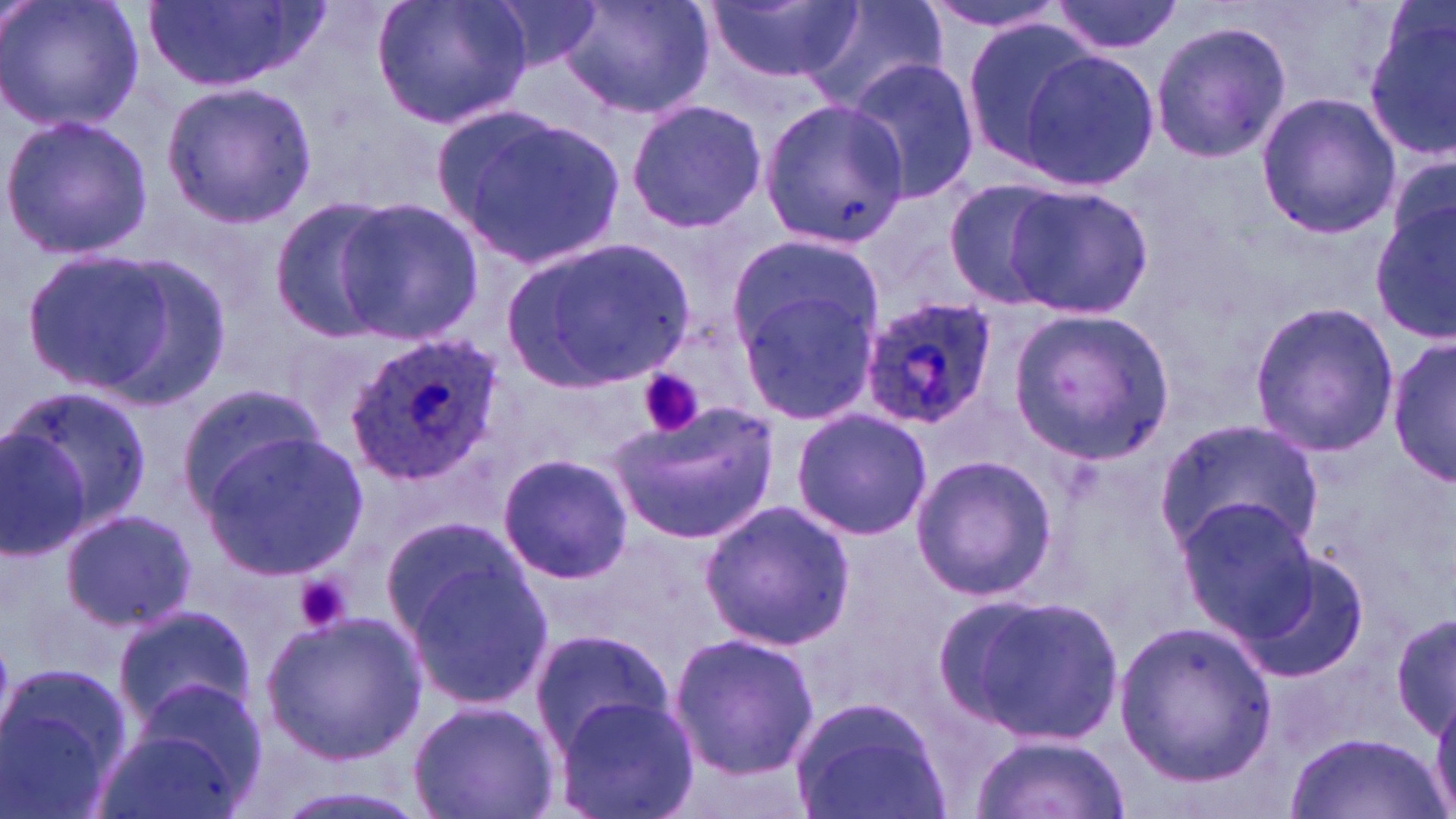
Summary:
  - Coordinate format: approximate bounding boxes as (x1, y1, x2, y2) in pixels
  - Uninfected red blood cell locations: (0, 0, 147, 135), (143, 0, 322, 94), (372, 0, 532, 132), (479, 0, 604, 71), (560, 0, 713, 121), (709, 0, 858, 88), (797, 0, 947, 117), (921, 0, 1079, 35), (1050, 0, 1183, 57), (1364, 4, 1456, 158), (1150, 19, 1290, 165), (962, 21, 1106, 175), (1016, 47, 1161, 193), (843, 57, 982, 203), (160, 81, 319, 226), (1254, 91, 1399, 239), (626, 97, 768, 234), (757, 98, 907, 242), (437, 107, 630, 274), (1, 113, 156, 259), (1385, 149, 1456, 274), (941, 178, 1072, 309), (1003, 184, 1152, 320), (268, 193, 398, 341), (333, 197, 483, 346), (1373, 202, 1456, 348), (726, 231, 882, 361), (505, 239, 698, 393), (16, 245, 218, 404), (737, 287, 880, 424), (1245, 299, 1399, 457), (1007, 310, 1174, 463), (1389, 335, 1454, 487), (174, 382, 327, 516), (7, 385, 151, 537), (611, 401, 782, 542), (790, 407, 933, 540), (1157, 417, 1322, 562), (0, 421, 92, 559), (202, 433, 368, 579), (910, 453, 1058, 602), (497, 454, 634, 583), (1173, 497, 1319, 649), (699, 500, 854, 651), (60, 506, 196, 634), (379, 513, 528, 647), (391, 543, 558, 710), (1234, 550, 1373, 682), (945, 593, 1125, 745), (1390, 603, 1454, 747), (114, 604, 257, 731), (261, 611, 425, 763), (1113, 620, 1279, 790), (529, 628, 673, 755), (666, 629, 818, 778), (1, 663, 130, 817), (550, 696, 698, 819), (790, 696, 952, 819), (409, 700, 558, 819), (97, 709, 254, 819), (1287, 730, 1440, 818), (971, 732, 1131, 819), (265, 781, 431, 819)
  - Platelet locations: (638, 368, 705, 439), (293, 573, 352, 635)
  - Plasmodium ovale-infected red blood cell locations: (857, 295, 1000, 429), (341, 330, 505, 489)
  - Slide-level diagnosis: Plasmodium ovale
  - Magnification: 1000x
  - Image size: 1456×819 pixels
  - Preparation: thin blood film
  - Field of view: one of a larger specimen
  - Stain: May-Grünwald-Giemsa
  - Modality: optical microscopy